Outline each blood parasite and name the species.
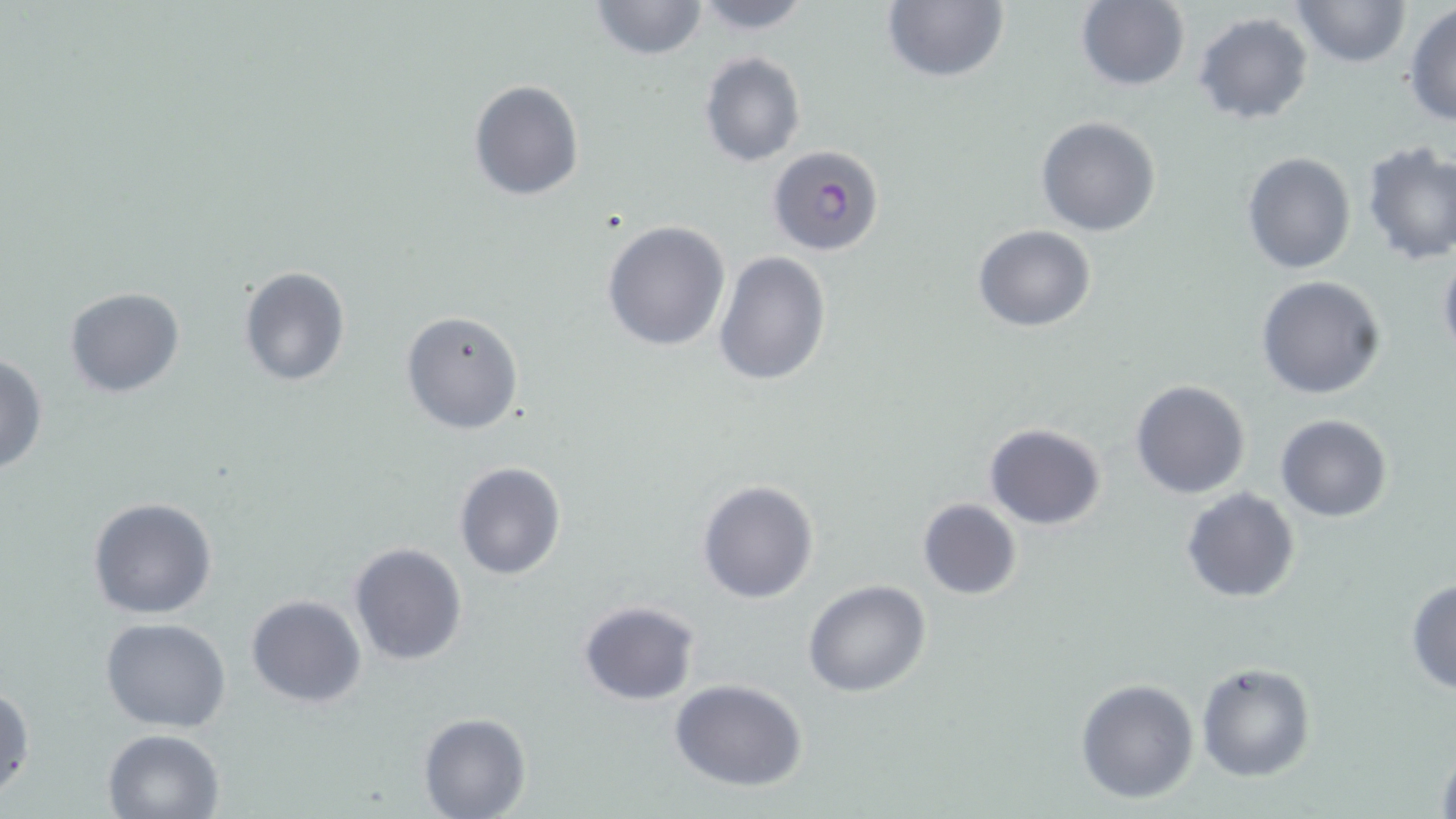
Approximate bounding boxes as [x1, y1, x2, y2] in pixels.
Plasmodium falciparum-infected red blood cells: [769, 144, 886, 258].
No Plasmodium ovale, Plasmodium malariae, Plasmodium vivax, Babesia divergens, or Trypanosoma brucei observed.

Summary:
  - Uninfected red blood cell locations: [590, 0, 708, 62], [686, 0, 816, 34], [1074, 0, 1191, 91], [1289, 0, 1413, 69], [882, 1, 1008, 83], [1404, 4, 1456, 126], [1192, 12, 1314, 125], [697, 50, 807, 168], [468, 80, 584, 201], [1035, 117, 1162, 238], [1360, 141, 1455, 266], [1241, 152, 1357, 275], [601, 221, 731, 353], [972, 224, 1096, 331], [1437, 246, 1456, 368], [713, 251, 832, 387], [239, 266, 350, 386], [1256, 275, 1387, 399], [64, 285, 187, 398], [401, 308, 525, 434], [0, 352, 49, 476], [1128, 378, 1252, 500], [1275, 414, 1392, 523], [983, 422, 1108, 531], [452, 461, 566, 579], [697, 480, 820, 604], [1181, 488, 1299, 604], [86, 496, 219, 621], [916, 498, 1022, 600], [348, 542, 469, 666], [802, 578, 931, 698], [1405, 578, 1456, 694], [246, 595, 366, 709], [578, 600, 701, 706], [100, 618, 232, 733], [1196, 662, 1318, 782], [667, 679, 810, 790], [1076, 679, 1200, 805], [0, 683, 34, 803], [418, 713, 531, 819], [102, 728, 225, 818], [1432, 739, 1456, 819]
  - Slide-level diagnosis: Plasmodium falciparum
  - Modality: light microscopy
  - Stain: May-Grünwald-Giemsa
  - Magnification: 1000x
  - Field of view: one of a larger specimen
  - Preparation: thin blood smear
  - Image size: 1456×819 pixels